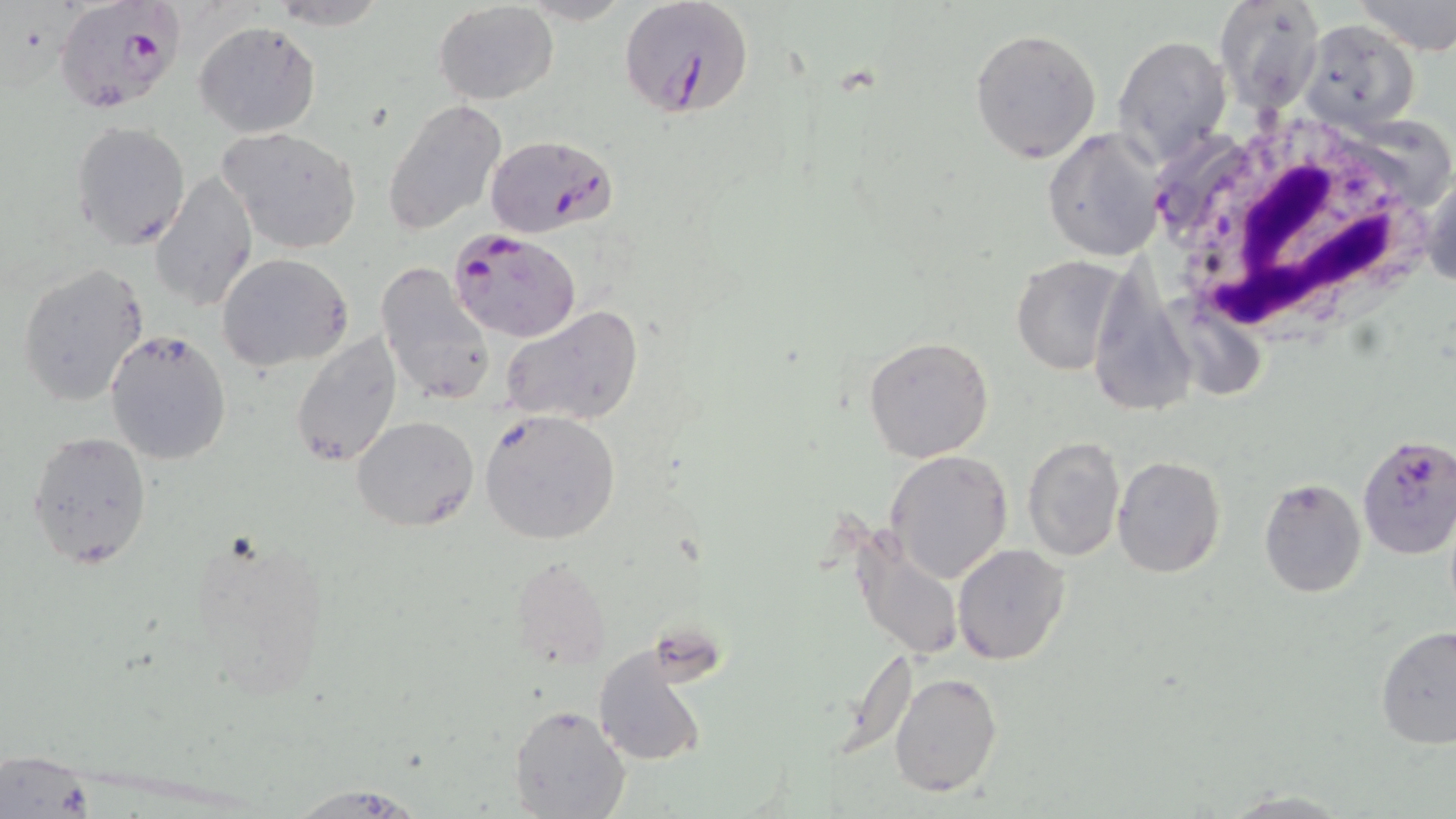

{
  "slide_level_diagnosis": "Plasmodium falciparum",
  "field_of_view": "one of a larger specimen",
  "stain": "May-Grünwald-Giemsa",
  "preparation": "thin blood film",
  "white_blood_cell_locations": "approximate bounding boxes as (x1, y1, x2, y2) in pixels: (1150, 106, 1444, 338)",
  "modality": "light microscopy",
  "magnification": "1000x",
  "plasmodium_falciparum_infected_red_blood_cell_locations": "approximate bounding boxes as (x1, y1, x2, y2) in pixels: (619, 0, 754, 123), (58, 4, 185, 114), (1296, 19, 1420, 131), (1149, 129, 1248, 235), (486, 134, 616, 239), (449, 228, 582, 344), (1355, 435, 1456, 557)",
  "uninfected_red_blood_cell_locations": "approximate bounding boxes as (x1, y1, x2, y2) in pixels: (264, 0, 390, 28), (1351, 0, 1456, 55), (1216, 1, 1328, 113), (433, 2, 558, 104), (194, 20, 321, 138), (970, 26, 1101, 164), (1113, 33, 1232, 168), (382, 98, 508, 234), (69, 120, 193, 251), (216, 126, 363, 253), (1043, 128, 1166, 262), (1421, 162, 1455, 301), (149, 172, 257, 313), (216, 253, 352, 372), (1011, 255, 1125, 375), (375, 261, 496, 408), (17, 262, 150, 407), (500, 305, 643, 428), (106, 330, 233, 468), (290, 331, 405, 470), (864, 335, 995, 463), (479, 408, 623, 546), (352, 415, 477, 532), (27, 431, 152, 568), (1021, 436, 1126, 563), (884, 450, 1013, 583), (1113, 455, 1226, 578), (1257, 477, 1368, 598), (848, 527, 965, 662), (952, 543, 1071, 665), (507, 557, 610, 671), (1375, 626, 1456, 750), (594, 644, 709, 768), (887, 672, 1003, 798), (511, 705, 632, 819), (2, 751, 98, 819), (280, 784, 428, 818), (1217, 789, 1356, 819)",
  "image_size": "1456×819 pixels"
}